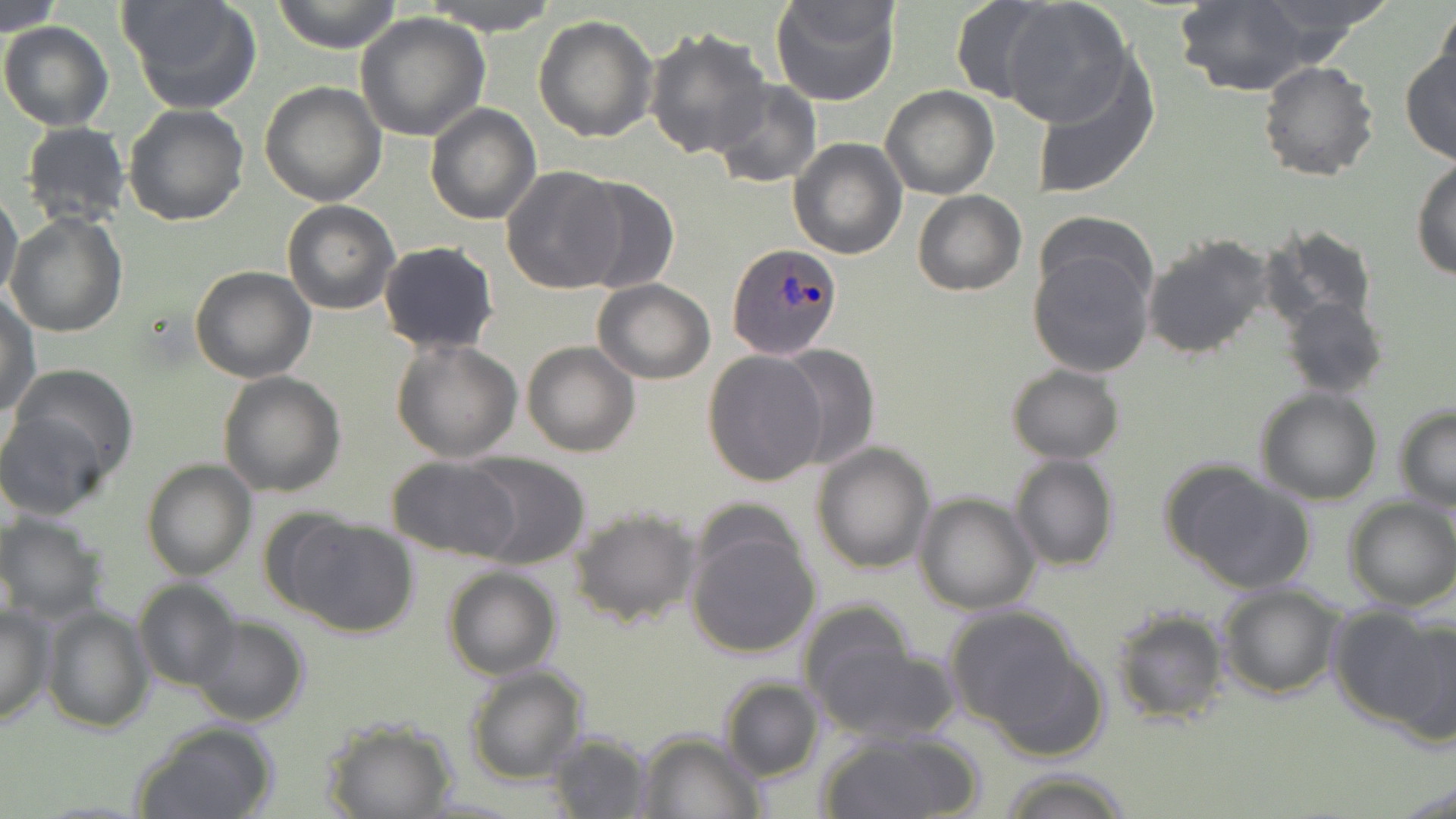
slide-level diagnosis = Plasmodium ovale
image size = 1456×819 pixels
preparation = thin blood film
stain = May-Grünwald-Giemsa
field of view = single
magnification = 1000x
uninfected red blood cell locations = approximate bounding boxes as named x1/y1/x2/y2 corners in pixels: (x1=119, y1=0, x2=262, y2=114), (x1=270, y1=0, x2=404, y2=53), (x1=416, y1=0, x2=565, y2=34), (x1=770, y1=0, x2=900, y2=108), (x1=1000, y1=0, x2=1135, y2=127), (x1=1175, y1=0, x2=1314, y2=95), (x1=949, y1=1, x2=1058, y2=101), (x1=0, y1=3, x2=66, y2=34), (x1=1435, y1=8, x2=1456, y2=96), (x1=356, y1=11, x2=491, y2=140), (x1=532, y1=14, x2=657, y2=141), (x1=1, y1=22, x2=115, y2=130), (x1=644, y1=27, x2=772, y2=159), (x1=1400, y1=48, x2=1456, y2=164), (x1=1028, y1=54, x2=1160, y2=201), (x1=1259, y1=61, x2=1380, y2=182), (x1=709, y1=80, x2=822, y2=189), (x1=259, y1=81, x2=387, y2=207), (x1=882, y1=85, x2=999, y2=199), (x1=123, y1=103, x2=251, y2=225), (x1=425, y1=103, x2=541, y2=225), (x1=19, y1=122, x2=131, y2=228), (x1=788, y1=138, x2=907, y2=259), (x1=1412, y1=158, x2=1456, y2=281), (x1=502, y1=165, x2=625, y2=295), (x1=570, y1=175, x2=680, y2=294), (x1=0, y1=189, x2=23, y2=303), (x1=912, y1=190, x2=1025, y2=295), (x1=282, y1=200, x2=399, y2=314), (x1=6, y1=212, x2=129, y2=338), (x1=1263, y1=225, x2=1378, y2=332), (x1=1140, y1=232, x2=1279, y2=361), (x1=378, y1=240, x2=499, y2=355), (x1=1028, y1=243, x2=1155, y2=378), (x1=190, y1=265, x2=317, y2=383), (x1=591, y1=279, x2=715, y2=384), (x1=1, y1=293, x2=40, y2=419), (x1=1279, y1=295, x2=1388, y2=398), (x1=392, y1=337, x2=523, y2=461), (x1=522, y1=341, x2=640, y2=457), (x1=775, y1=345, x2=880, y2=471), (x1=702, y1=349, x2=828, y2=488), (x1=5, y1=362, x2=141, y2=493), (x1=1007, y1=364, x2=1124, y2=464), (x1=218, y1=372, x2=346, y2=496), (x1=1255, y1=388, x2=1384, y2=506), (x1=1394, y1=405, x2=1456, y2=512), (x1=0, y1=407, x2=114, y2=521), (x1=811, y1=441, x2=936, y2=573), (x1=463, y1=454, x2=593, y2=568), (x1=1010, y1=454, x2=1118, y2=571), (x1=384, y1=457, x2=523, y2=561), (x1=141, y1=458, x2=256, y2=580), (x1=1162, y1=460, x2=1315, y2=594), (x1=914, y1=491, x2=1040, y2=613), (x1=1343, y1=497, x2=1456, y2=611), (x1=569, y1=505, x2=702, y2=628), (x1=0, y1=511, x2=109, y2=623), (x1=273, y1=513, x2=419, y2=637), (x1=684, y1=516, x2=823, y2=660), (x1=442, y1=566, x2=562, y2=680), (x1=134, y1=579, x2=242, y2=690), (x1=1216, y1=582, x2=1344, y2=699), (x1=795, y1=601, x2=920, y2=722), (x1=0, y1=602, x2=54, y2=729), (x1=42, y1=604, x2=155, y2=735), (x1=943, y1=607, x2=1089, y2=735), (x1=1110, y1=607, x2=1230, y2=725), (x1=1353, y1=608, x2=1456, y2=743), (x1=188, y1=616, x2=311, y2=727), (x1=813, y1=640, x2=961, y2=745), (x1=464, y1=666, x2=588, y2=784), (x1=721, y1=678, x2=824, y2=781), (x1=320, y1=718, x2=458, y2=819), (x1=131, y1=721, x2=280, y2=819), (x1=820, y1=730, x2=984, y2=819), (x1=546, y1=731, x2=653, y2=817), (x1=636, y1=731, x2=764, y2=818), (x1=997, y1=767, x2=1131, y2=818)
modality = light microscopy
Plasmodium ovale-infected red blood cell locations = approximate bounding boxes as named x1/y1/x2/y2 corners in pixels: (x1=728, y1=243, x2=843, y2=358)